Identify the blood parasite species.
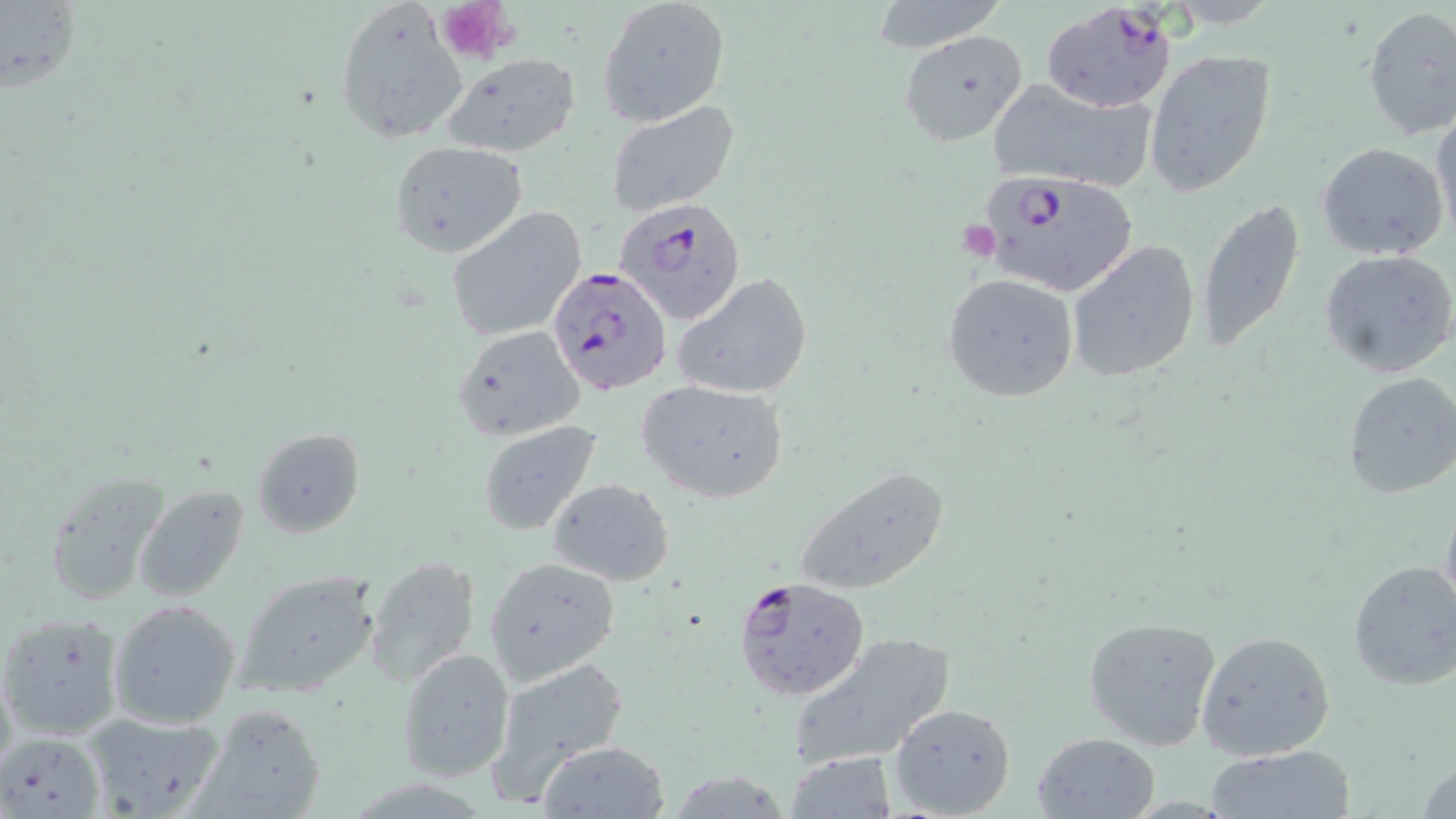

Plasmodium falciparum.

platelet_locations: 'approximate bounding boxes as named x1/y1/x2/y2 corners in pixels: (x1=436, y1=0, x2=518, y2=64)'
modality: optical microscopy
field_of_view: one of a larger specimen
uninfected_red_blood_cell_locations: 'approximate bounding boxes as named x1/y1/x2/y2 corners in pixels: (x1=863, y1=0, x2=1011, y2=53), (x1=1, y1=1, x2=82, y2=94), (x1=333, y1=1, x2=467, y2=145), (x1=596, y1=1, x2=730, y2=127), (x1=1360, y1=6, x2=1456, y2=141), (x1=901, y1=32, x2=1028, y2=145), (x1=1142, y1=51, x2=1277, y2=197), (x1=442, y1=53, x2=582, y2=158), (x1=984, y1=82, x2=1154, y2=192), (x1=606, y1=103, x2=742, y2=221), (x1=1432, y1=103, x2=1456, y2=245), (x1=390, y1=141, x2=528, y2=258), (x1=1317, y1=143, x2=1450, y2=262), (x1=1195, y1=199, x2=1306, y2=352), (x1=447, y1=205, x2=587, y2=341), (x1=1066, y1=239, x2=1202, y2=383), (x1=1318, y1=248, x2=1456, y2=379), (x1=941, y1=272, x2=1078, y2=402), (x1=673, y1=273, x2=814, y2=400), (x1=452, y1=325, x2=587, y2=444), (x1=1341, y1=372, x2=1456, y2=501), (x1=634, y1=380, x2=787, y2=502), (x1=477, y1=421, x2=602, y2=536), (x1=252, y1=428, x2=366, y2=536), (x1=792, y1=464, x2=953, y2=596), (x1=44, y1=466, x2=174, y2=605), (x1=545, y1=477, x2=676, y2=587), (x1=513, y1=482, x2=659, y2=665), (x1=134, y1=485, x2=252, y2=602), (x1=1439, y1=487, x2=1456, y2=628), (x1=485, y1=555, x2=620, y2=684), (x1=365, y1=558, x2=479, y2=687), (x1=1348, y1=560, x2=1456, y2=690), (x1=238, y1=571, x2=378, y2=695), (x1=109, y1=599, x2=241, y2=729), (x1=0, y1=613, x2=125, y2=741), (x1=1081, y1=614, x2=1221, y2=751), (x1=1195, y1=630, x2=1336, y2=760), (x1=784, y1=631, x2=955, y2=769), (x1=395, y1=648, x2=515, y2=783), (x1=490, y1=656, x2=628, y2=807), (x1=889, y1=702, x2=1017, y2=817), (x1=190, y1=703, x2=327, y2=817), (x1=81, y1=709, x2=228, y2=819), (x1=1032, y1=730, x2=1161, y2=819), (x1=4, y1=732, x2=103, y2=818), (x1=535, y1=739, x2=669, y2=817), (x1=1205, y1=745, x2=1356, y2=819), (x1=786, y1=752, x2=896, y2=817), (x1=1416, y1=756, x2=1456, y2=819)'
plasmodium_falciparum_infected_red_blood_cell_locations: 'approximate bounding boxes as named x1/y1/x2/y2 corners in pixels: (x1=1040, y1=3, x2=1177, y2=113), (x1=975, y1=169, x2=1138, y2=297), (x1=614, y1=197, x2=748, y2=324), (x1=548, y1=266, x2=674, y2=397), (x1=732, y1=575, x2=871, y2=701)'
image_size: 1456×819 pixels
stain: May-Grünwald-Giemsa
preparation: thin blood film
magnification: 1000x